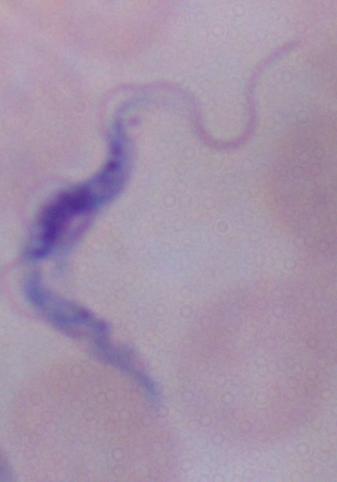

identification = trypanosome
magnification = 1000x
modality = micrograph